Locate every leukocyte (white blood cell).
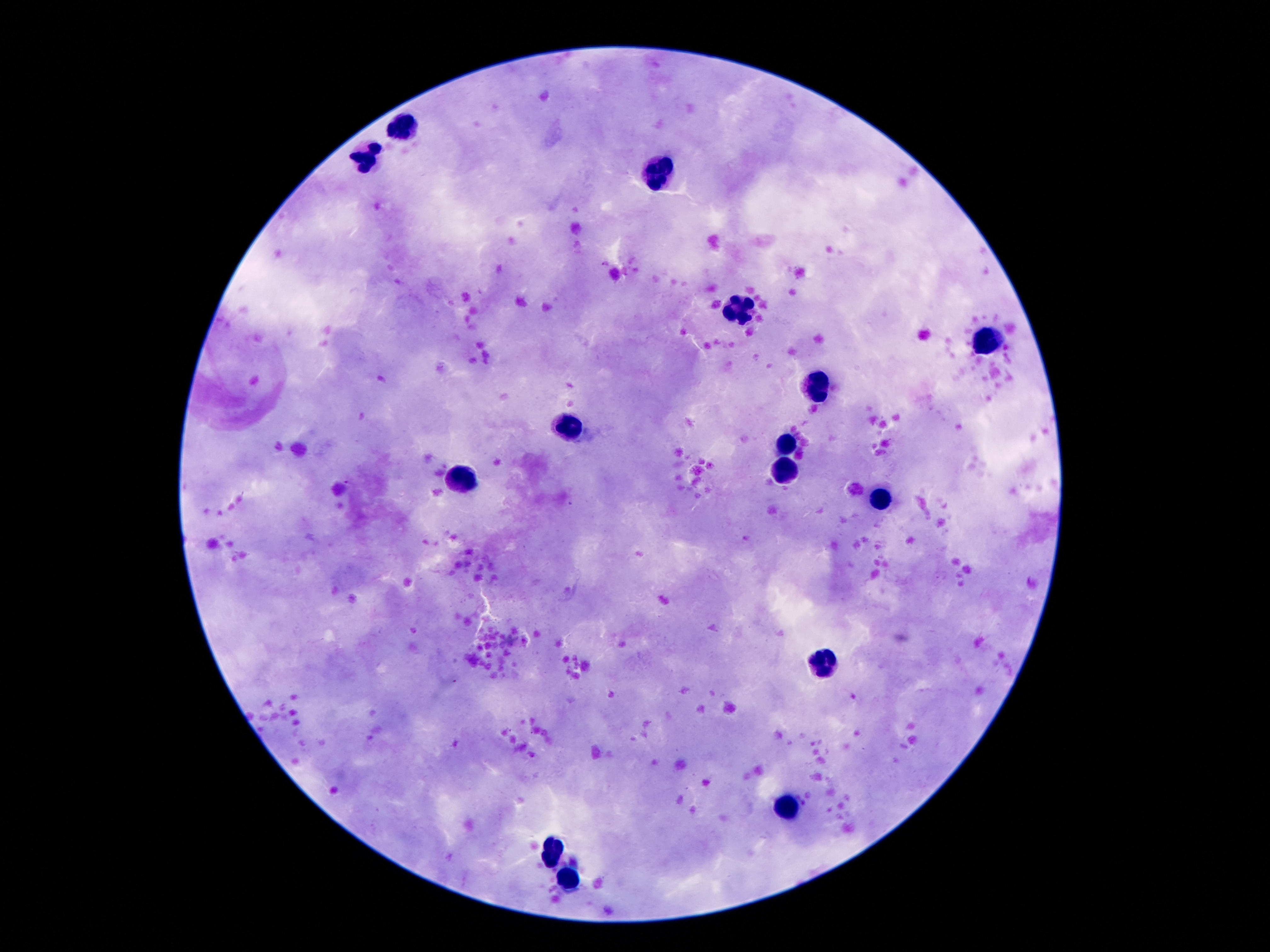
Approximate object centers, in pixels from the top-left corner.
Leukocytes: (x=410, y=125), (x=370, y=156), (x=658, y=167), (x=739, y=309), (x=985, y=340), (x=821, y=391), (x=574, y=424), (x=788, y=443), (x=784, y=472), (x=467, y=479), (x=885, y=497), (x=823, y=662), (x=788, y=802), (x=549, y=855), (x=571, y=881).

{
  "preparation": "thick peripheral-blood smear",
  "patient_malaria_status": "not infected",
  "magnification": "100x",
  "field_of_view": "single",
  "stain": "Giemsa",
  "capture": "smartphone camera through the microscope eyepiece",
  "image_size": "1270×952 pixels"
}